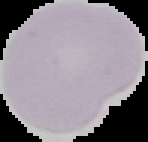
From a thin blood film. Segmented cell region on a black background. Image is 148×142 pixels. Result: negative for malaria parasites.